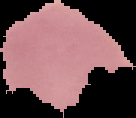

malaria status = parasitized
image type = segmented cell region on a black background
preparation = thin blood smear
image size = 136×118 pixels